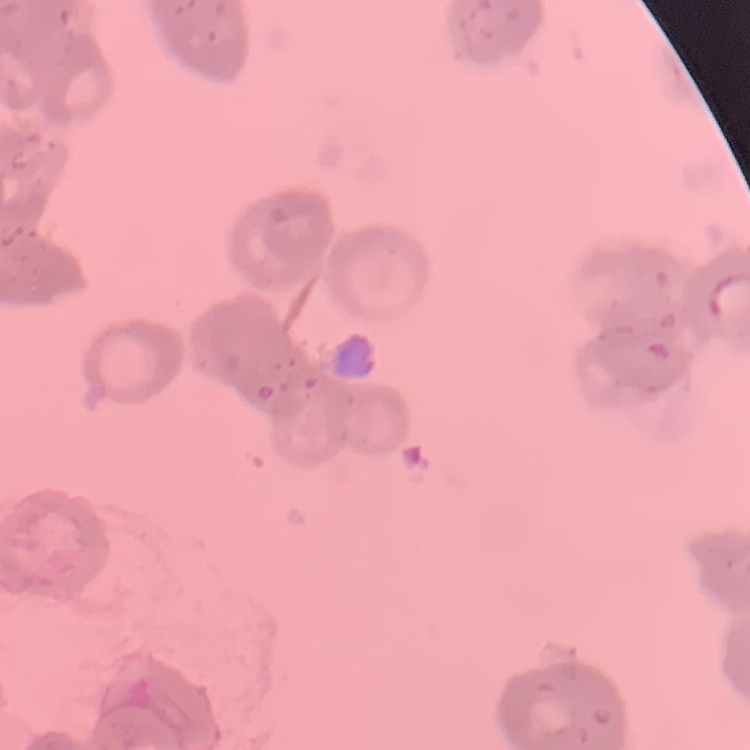 The red blood cells show rouleaux formation. Field's or Giemsa stain. Thin peripheral smear. One tile cut from a larger photomicrograph.